Name the blood parasite species.
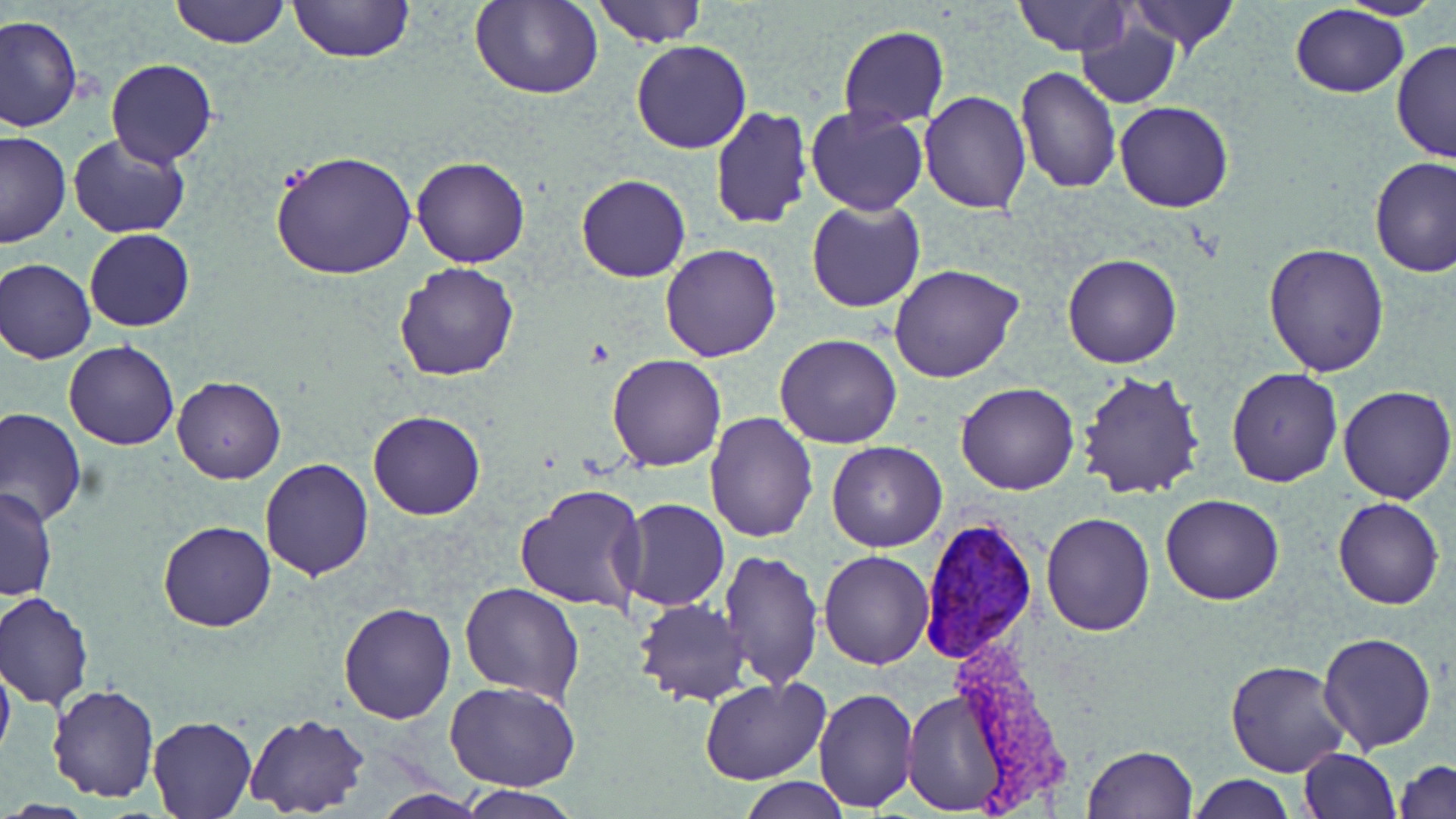
Plasmodium vivax.

Approximate bounding boxes as named x1/y1/x2/y2 corners in pixels. Plasmodium vivax-infected red blood cell locations: (x1=918, y1=512, x2=1040, y2=667). Uninfected red blood cell locations: (x1=169, y1=0, x2=289, y2=48), (x1=289, y1=0, x2=413, y2=65), (x1=595, y1=0, x2=707, y2=48), (x1=1012, y1=0, x2=1134, y2=56), (x1=1127, y1=0, x2=1240, y2=53), (x1=1338, y1=0, x2=1442, y2=20), (x1=469, y1=2, x2=604, y2=100), (x1=1290, y1=4, x2=1411, y2=97), (x1=1, y1=14, x2=83, y2=132), (x1=1076, y1=16, x2=1182, y2=109), (x1=837, y1=25, x2=949, y2=128), (x1=1391, y1=38, x2=1455, y2=163), (x1=629, y1=40, x2=753, y2=154), (x1=105, y1=59, x2=218, y2=165), (x1=1015, y1=64, x2=1121, y2=194), (x1=919, y1=90, x2=1031, y2=213), (x1=1115, y1=101, x2=1234, y2=213), (x1=805, y1=105, x2=929, y2=216), (x1=709, y1=106, x2=813, y2=230), (x1=0, y1=129, x2=71, y2=247), (x1=68, y1=133, x2=194, y2=238), (x1=271, y1=149, x2=417, y2=282), (x1=411, y1=155, x2=531, y2=270), (x1=1369, y1=156, x2=1456, y2=277), (x1=575, y1=173, x2=691, y2=283), (x1=806, y1=198, x2=925, y2=313), (x1=84, y1=228, x2=196, y2=331), (x1=1264, y1=242, x2=1388, y2=377), (x1=660, y1=244, x2=782, y2=364), (x1=1062, y1=253, x2=1183, y2=369), (x1=0, y1=257, x2=96, y2=363), (x1=394, y1=262, x2=521, y2=382), (x1=888, y1=264, x2=1025, y2=384), (x1=774, y1=333, x2=902, y2=449), (x1=64, y1=341, x2=179, y2=450), (x1=606, y1=355, x2=727, y2=472), (x1=1226, y1=367, x2=1343, y2=487), (x1=1077, y1=369, x2=1206, y2=501), (x1=172, y1=375, x2=285, y2=484), (x1=954, y1=383, x2=1079, y2=496), (x1=1336, y1=384, x2=1455, y2=503), (x1=1, y1=408, x2=86, y2=526), (x1=368, y1=409, x2=486, y2=520), (x1=704, y1=410, x2=818, y2=542), (x1=825, y1=441, x2=947, y2=552), (x1=259, y1=458, x2=374, y2=580), (x1=514, y1=481, x2=647, y2=612), (x1=1, y1=487, x2=57, y2=602), (x1=1160, y1=493, x2=1286, y2=605), (x1=1333, y1=496, x2=1443, y2=610), (x1=618, y1=498, x2=730, y2=612), (x1=1041, y1=512, x2=1155, y2=636), (x1=157, y1=520, x2=276, y2=633), (x1=719, y1=549, x2=823, y2=689), (x1=818, y1=549, x2=935, y2=670), (x1=460, y1=581, x2=584, y2=702), (x1=2, y1=592, x2=93, y2=708), (x1=634, y1=598, x2=750, y2=707), (x1=336, y1=602, x2=456, y2=723), (x1=1318, y1=632, x2=1436, y2=753), (x1=0, y1=658, x2=15, y2=767), (x1=1225, y1=658, x2=1351, y2=776), (x1=699, y1=678, x2=830, y2=786), (x1=446, y1=680, x2=581, y2=793), (x1=47, y1=685, x2=161, y2=802), (x1=812, y1=687, x2=919, y2=812), (x1=900, y1=688, x2=1006, y2=813), (x1=244, y1=713, x2=370, y2=817), (x1=148, y1=716, x2=257, y2=817), (x1=1082, y1=745, x2=1197, y2=818), (x1=1299, y1=749, x2=1400, y2=819), (x1=1396, y1=759, x2=1456, y2=817), (x1=1188, y1=775, x2=1296, y2=818), (x1=739, y1=777, x2=852, y2=818), (x1=460, y1=786, x2=580, y2=818), (x1=372, y1=790, x2=490, y2=818). 1000x magnification. Image is 1456×819 pixels. One field of a larger specimen. Thin blood film. May-Grünwald-Giemsa stain. Light microscopy.